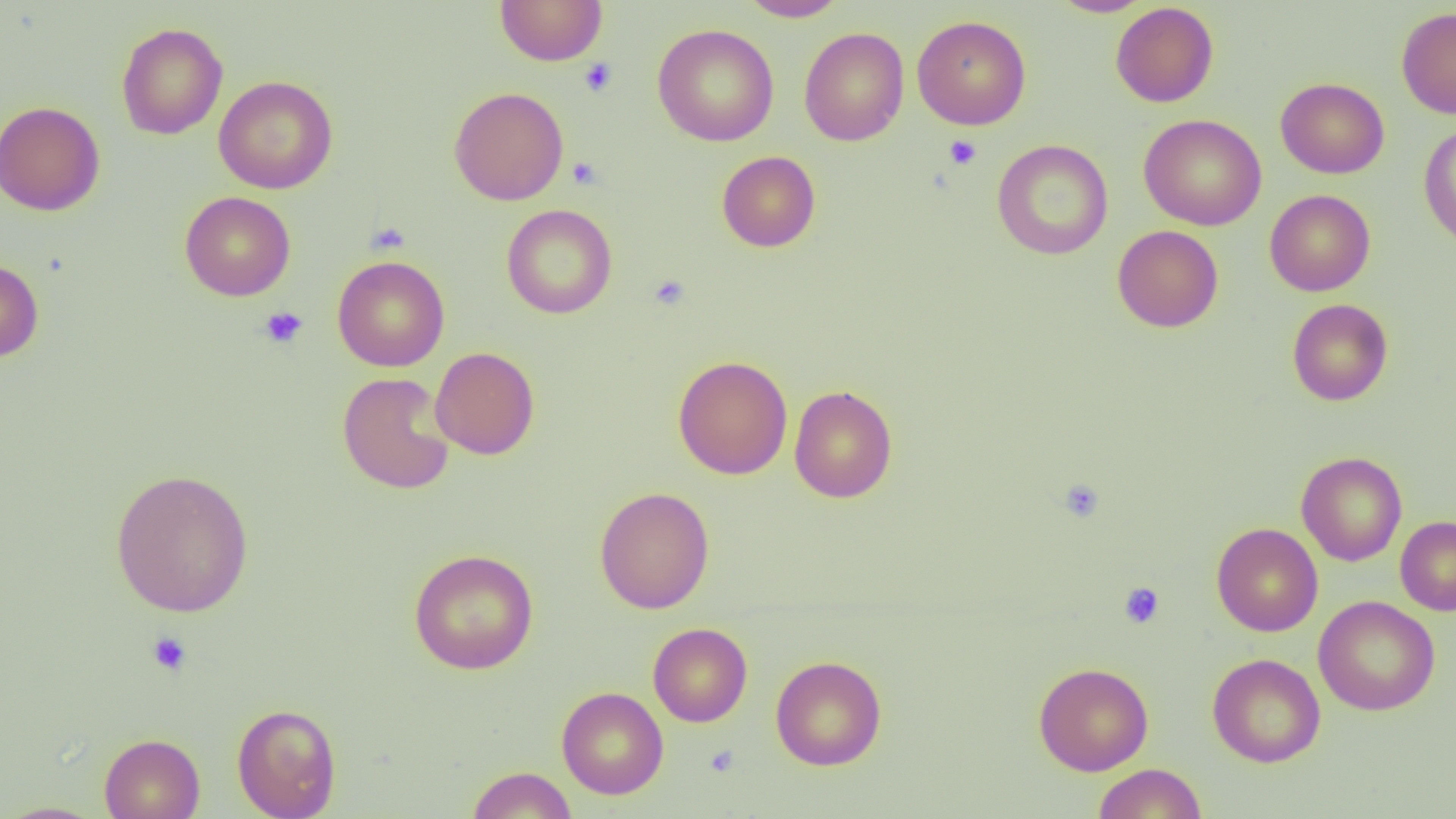

slide-level diagnosis = negative for blood parasites
preparation = thin blood film
image size = 1456×819 pixels
uninfected red blood cell locations = approximate bounding boxes as (x1,y1)-(x2,y2) corner pairs in pixels: (494,0)-(608,66), (736,0)-(847,21), (1049,0)-(1154,17), (1110,2)-(1219,107), (1396,7)-(1456,118), (912,14)-(1031,130), (116,22)-(228,140), (652,23)-(779,146), (798,27)-(909,146), (213,76)-(338,194), (1276,77)-(1390,178), (449,86)-(569,205), (0,101)-(105,216), (1139,114)-(1266,230), (1418,124)-(1456,251), (992,140)-(1113,260), (717,151)-(821,252), (1264,189)-(1376,296), (179,190)-(296,301), (502,204)-(618,319), (1112,225)-(1224,332), (332,255)-(450,371), (0,258)-(44,363), (1287,298)-(1393,405), (430,347)-(540,460), (672,355)-(793,479), (337,372)-(455,495), (788,385)-(897,503), (1296,451)-(1407,566), (110,467)-(254,617), (594,486)-(714,614), (1395,516)-(1456,615), (1211,522)-(1323,636), (408,548)-(539,674), (1313,595)-(1440,716), (648,622)-(753,727), (1207,652)-(1326,767), (770,655)-(887,770), (1033,662)-(1153,775), (556,686)-(669,799), (232,702)-(342,818), (99,733)-(205,819), (1092,763)-(1207,819), (467,766)-(578,819), (0,801)-(109,818)
modality = light microscopy
field of view = one of a larger specimen
platelet locations = approximate bounding boxes as (x1,y1)-(x2,y2) corner pairs in pixels: (496,1)-(605,65), (579,58)-(617,97), (944,135)-(982,170), (567,157)-(602,189), (648,274)-(691,311), (259,306)-(308,348), (1058,478)-(1105,522), (1119,582)-(1165,629), (146,631)-(192,677)
magnification = 1000x